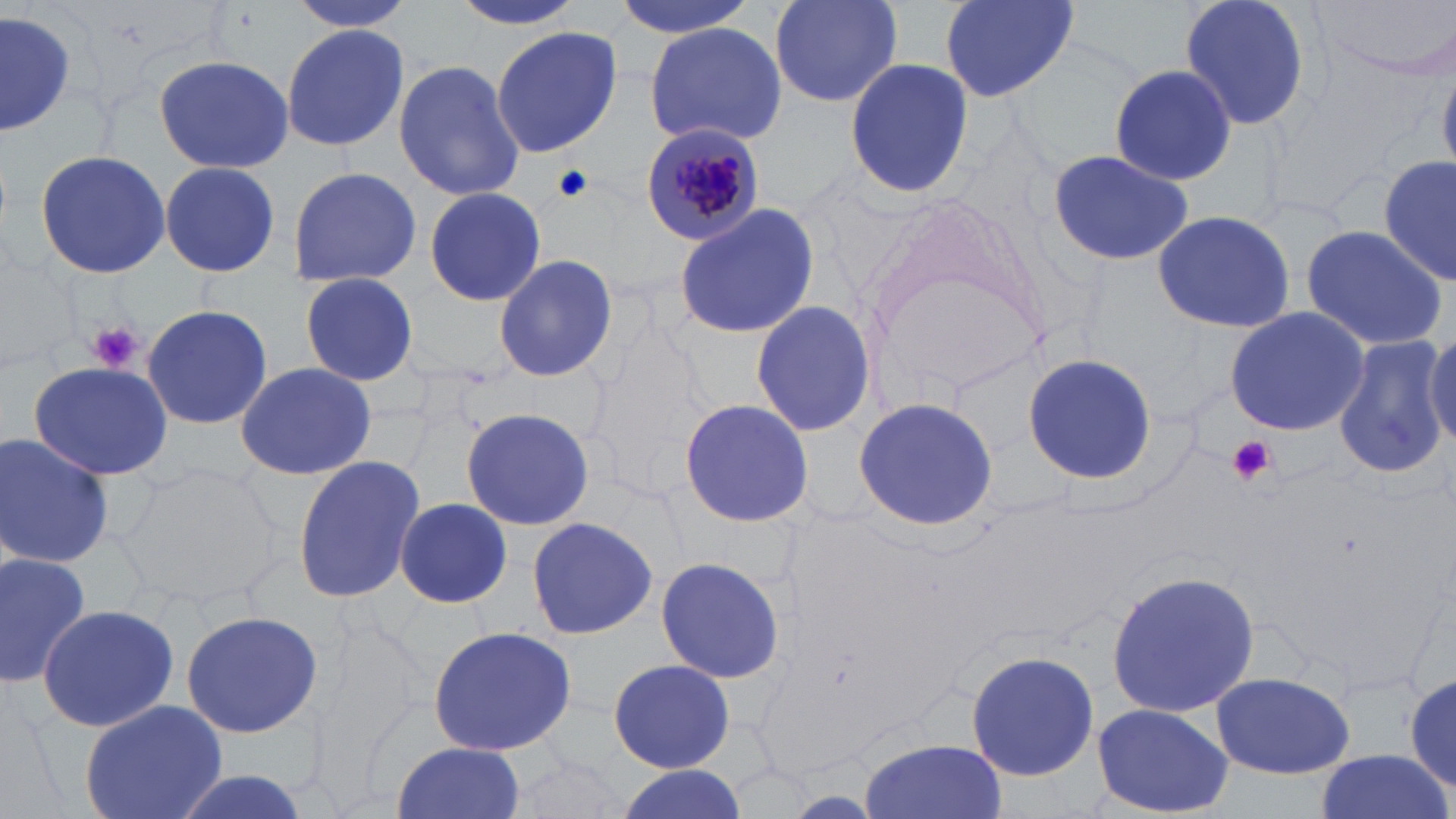
Summary:
  - Coordinate format: approximate bounding boxes as (x1, y1, x2, y2) in pixels
  - Plasmodium malariae-infected red blood cell locations: (639, 127, 763, 247)
  - Uninfected red blood cell locations: (285, 0, 422, 32), (450, 0, 589, 33), (609, 0, 756, 39), (767, 0, 906, 110), (935, 0, 1082, 103), (1174, 0, 1315, 135), (1314, 0, 1456, 80), (0, 8, 78, 141), (1114, 20, 1294, 167), (645, 21, 787, 149), (281, 22, 410, 153), (489, 24, 623, 158), (151, 56, 295, 173), (393, 58, 524, 203), (843, 58, 974, 199), (1106, 61, 1238, 186), (1046, 146, 1195, 269), (32, 149, 173, 281), (1379, 154, 1456, 286), (159, 161, 281, 278), (287, 165, 422, 286), (423, 185, 548, 307), (860, 199, 1055, 407), (673, 203, 820, 341), (1151, 208, 1296, 335), (1299, 224, 1448, 352), (0, 249, 80, 368), (492, 253, 619, 383), (296, 271, 420, 386), (749, 299, 878, 437), (141, 304, 273, 430), (1222, 307, 1371, 435), (586, 318, 708, 493), (1425, 330, 1456, 443), (1333, 335, 1451, 479), (1022, 351, 1156, 486), (28, 359, 173, 482), (233, 362, 377, 481), (851, 396, 1000, 532), (678, 397, 813, 529), (460, 406, 596, 532), (0, 431, 116, 572), (292, 455, 430, 604), (122, 461, 286, 607), (396, 498, 512, 607), (525, 516, 658, 641), (0, 549, 91, 685), (654, 556, 786, 685), (1104, 568, 1259, 720), (36, 602, 182, 734), (181, 608, 323, 738), (426, 625, 578, 757), (964, 649, 1099, 782), (607, 658, 736, 773), (1415, 668, 1455, 790), (1209, 670, 1355, 779), (79, 700, 226, 819), (1092, 702, 1235, 818), (858, 737, 1008, 819), (390, 740, 527, 819), (505, 746, 631, 819), (1312, 752, 1454, 819), (611, 763, 745, 819), (155, 767, 322, 819)
  - Platelet locations: (554, 164, 593, 202), (88, 322, 141, 372), (1224, 435, 1276, 485)
  - Slide-level diagnosis: Plasmodium malariae
  - Stain: May-Grünwald-Giemsa
  - Modality: light microscopy
  - Preparation: thin blood film
  - Field of view: one of a larger specimen
  - Image size: 1456×819 pixels
  - Magnification: 1000x